Point out each malaria parasite.
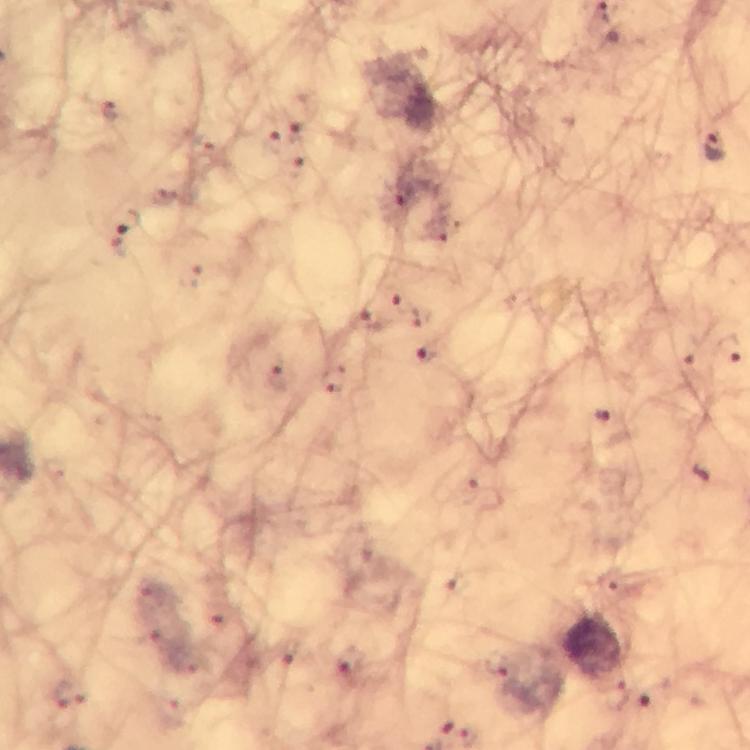
Approximate centers as {x, y} in pixels.
Malaria parasites: {110, 110}, {274, 141}, {712, 147}, {296, 167}, {398, 207}, {127, 221}, {405, 306}, {367, 320}, {727, 349}, {425, 358}, {277, 378}, {603, 418}, {348, 663}, {499, 666}, {618, 694}, {469, 738}.

Summary:
  - Preparation: thick blood smear
  - Image size: 750×750 pixels
  - Magnification: 100x
  - Capture: smartphone photograph through a microscope
  - Cropped from: one field of view
  - Immersion oil: applied
  - Stain: Giemsa
  - Context: from a malaria diagnostic workup